Name the cell type shown.
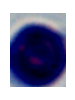

This is a leukocyte.

Summary:
  - Modality: micrograph
  - Magnification: 1000x